Classify this cell by malaria status.
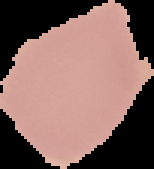

Uninfected.

The area outside the segmented cell region is set to black. From a thin blood film. Image is 154×169 pixels.